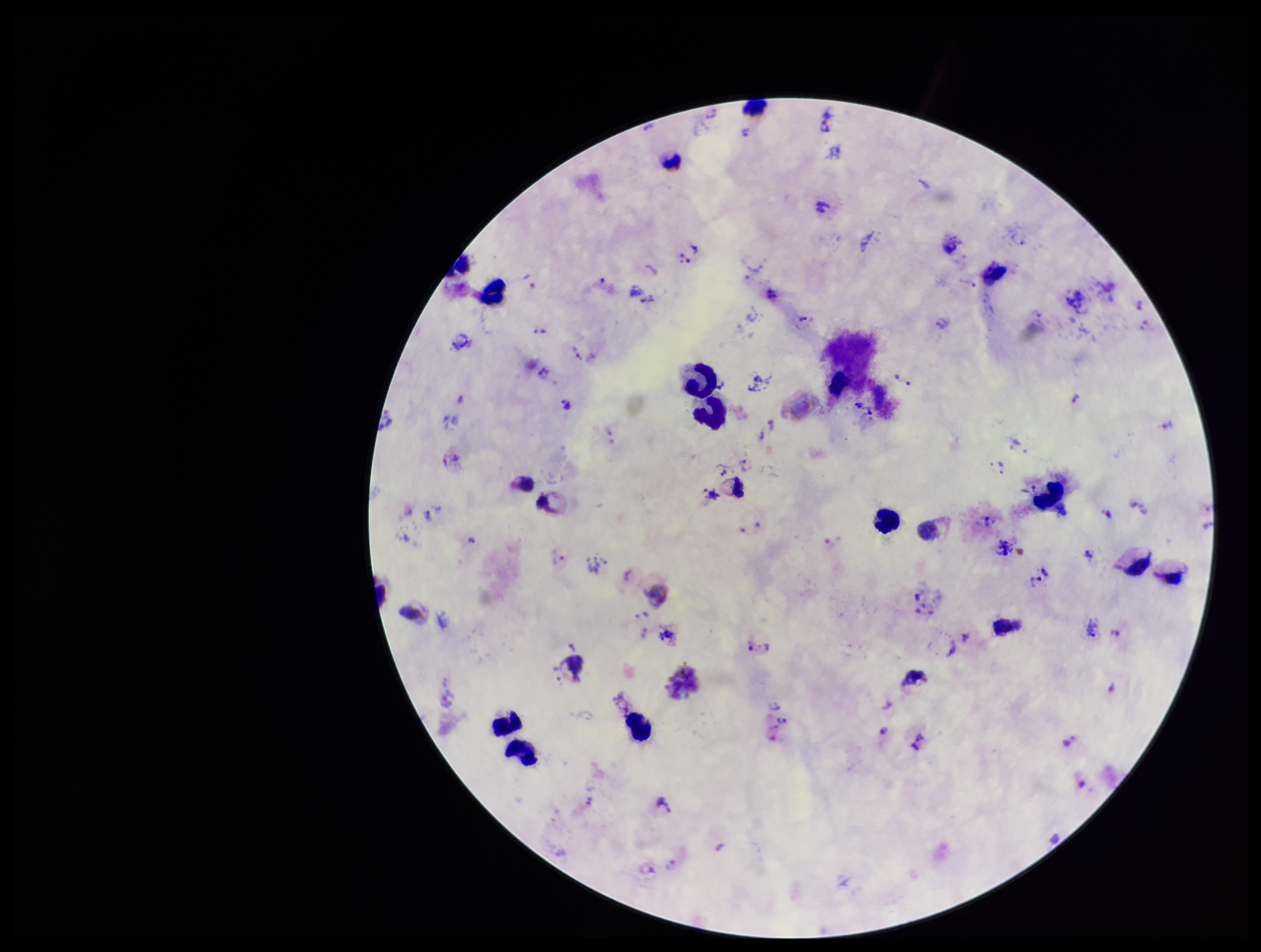

Patient malaria status: infected. Preparation: thick smear. Giemsa stain. Image is 1261×952 pixels. Parasite count: 46. Photographed through the microscope eyepiece with a smartphone camera. Plasmodium parasites: detected. Species reported for this patient: Plasmodium vivax. Leukocyte count: 14. Single field of view.